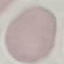
result: no malaria parasites seen
preparation: thin smear
capture: smartphone camera at the microscope eyepiece
image_type: automatically extracted cell patch, resized to 64 × 64 pixels
stain: Giemsa